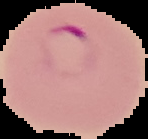
Summary:
  - Image size: 148×139 pixels
  - Image type: cell region segmented out of the field of view; surrounding area masked to black
  - Preparation: thin blood smear
  - Result: malaria parasites detected